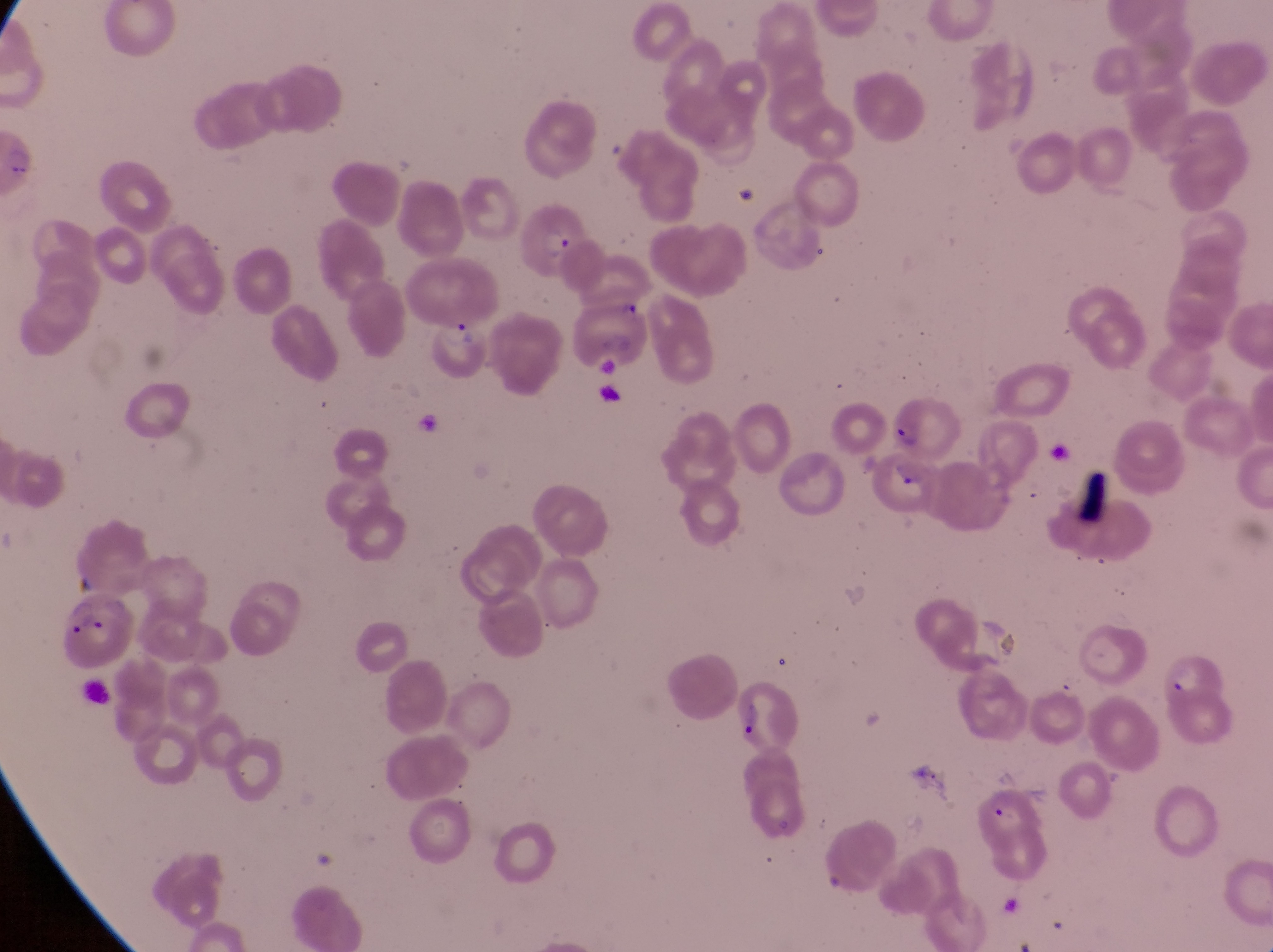
Approximate bounding boxes as (left, top, right, bottom) in pixels.
Summary:
  - Parasitised red blood cell locations: (517, 205, 587, 280), (424, 317, 486, 382), (894, 389, 964, 461), (874, 455, 937, 517), (52, 596, 135, 668), (732, 686, 799, 753)
  - Image size: 1273×952 pixels
  - Field of view: single
  - Magnification: 1000x
  - Country: Uganda
  - Preparation: thin blood smear
  - Capture: smartphone photograph through the eyepiece of an Olympus CX-23 microscope